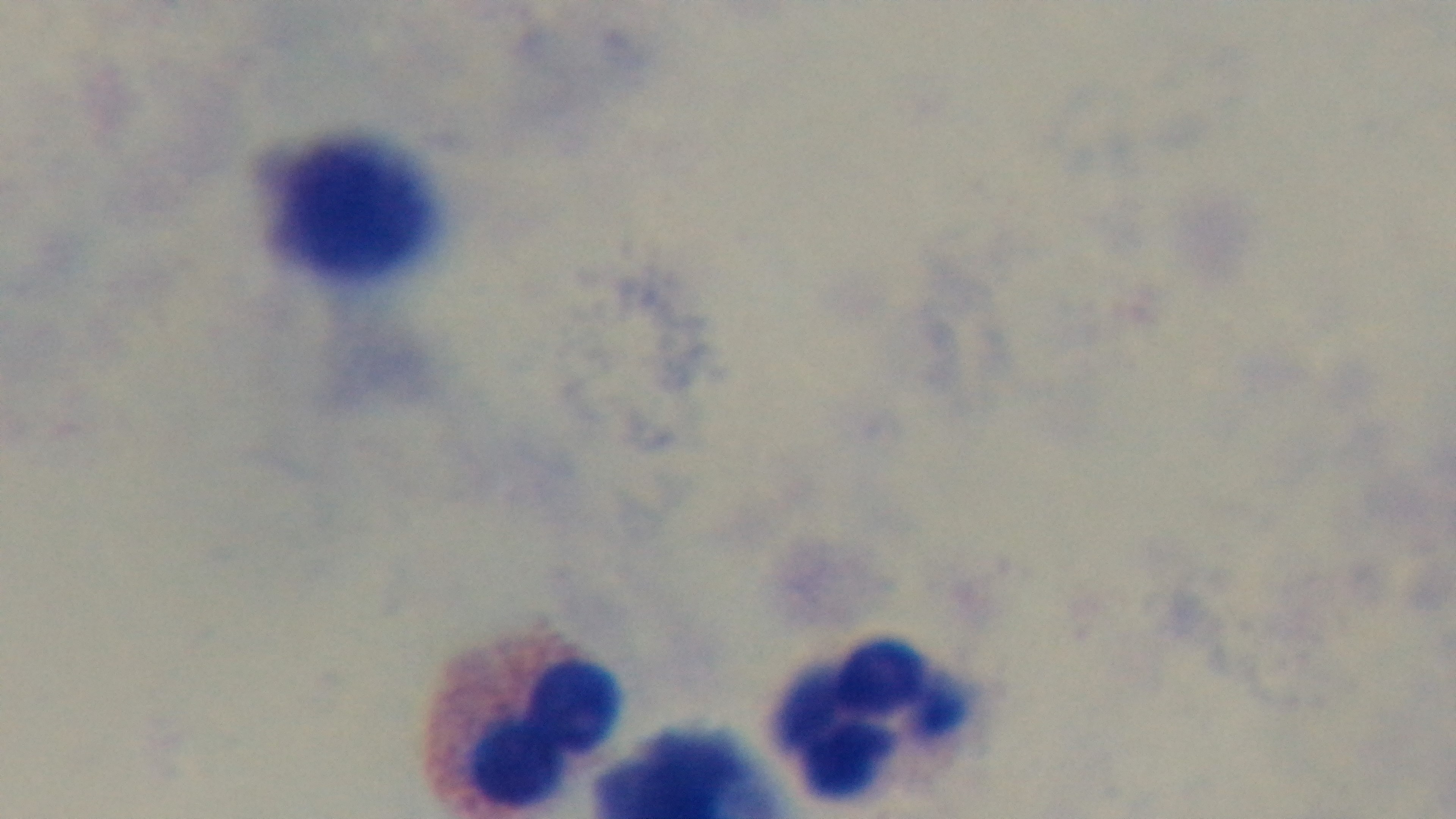
Mounted 4K digital camera. Oil-immersion objective, 100x. Photomicrograph. Single field of view. Preparation: thick smear. Malaria status: negative. Giemsa-stained.